Locate every Plasmodium parasite.
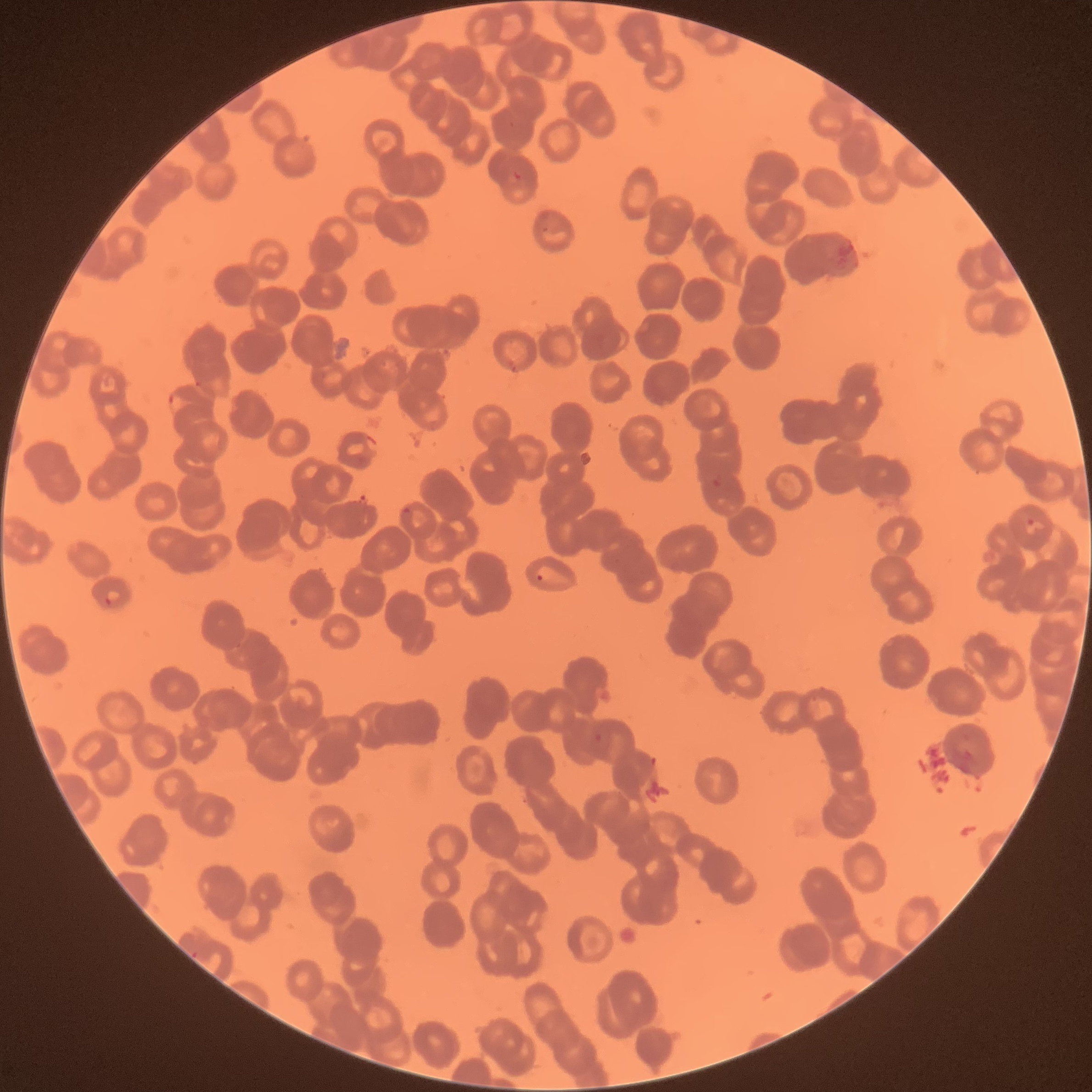
Approximate bounding boxes as [x1, y1, x2, y2] in pixels.
Plasmodium parasites: [511, 169, 523, 183], [168, 392, 187, 414], [712, 477, 723, 489], [399, 506, 413, 526], [1025, 516, 1036, 528], [536, 572, 544, 582], [105, 587, 123, 605], [592, 732, 603, 744].

Image is 1092×1092 pixels. Optical microscopy. Thin blood film. The red blood cells show rouleaux formation.